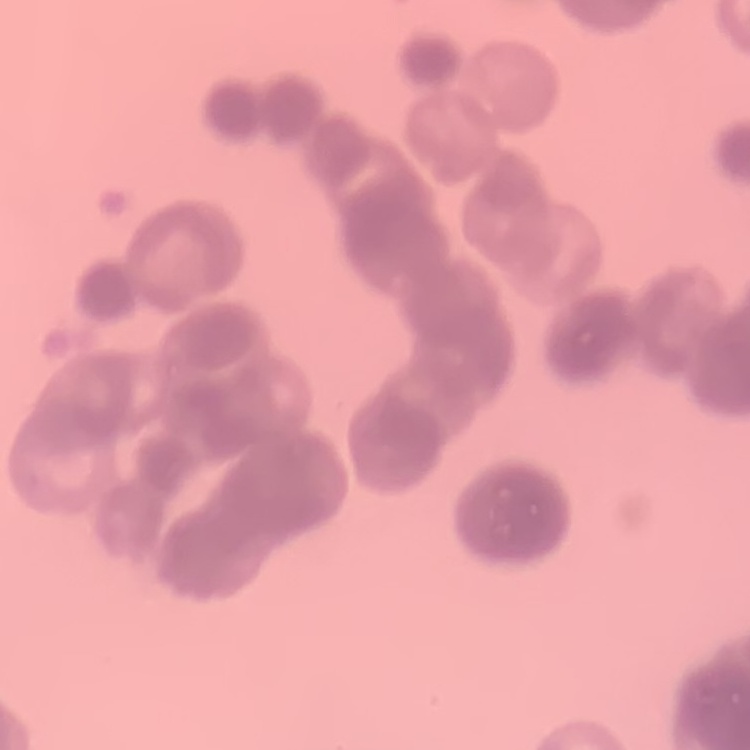

Summary:
  - Erythrocyte morphology: rouleaux formation
  - Stain: Field's or Giemsa
  - Image type: one tile cut from a larger photomicrograph
  - Preparation: thin blood smear